Point out each malaria parasite.
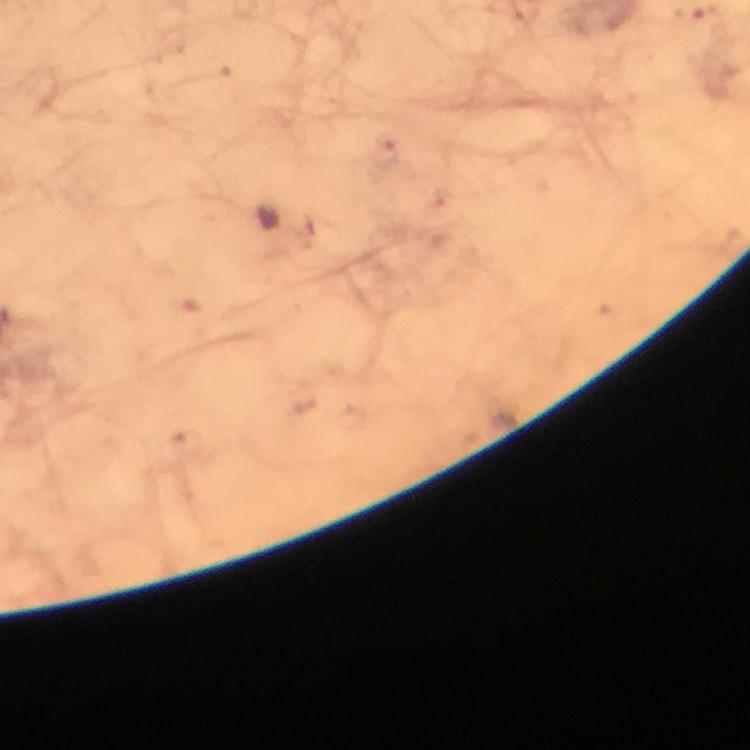
Approximate centers as (x, y) in pixels.
Malaria parasites: (388, 154).

Summary:
  - Cropped from: one field of view
  - Magnification: 100x
  - Capture: smartphone photograph through a microscope
  - Preparation: thick smear
  - Immersion oil: used
  - Stain: Giemsa
  - Image size: 750×750 pixels
  - Context: from a diagnostic examination for malaria